Locate and identify every blood parasite.
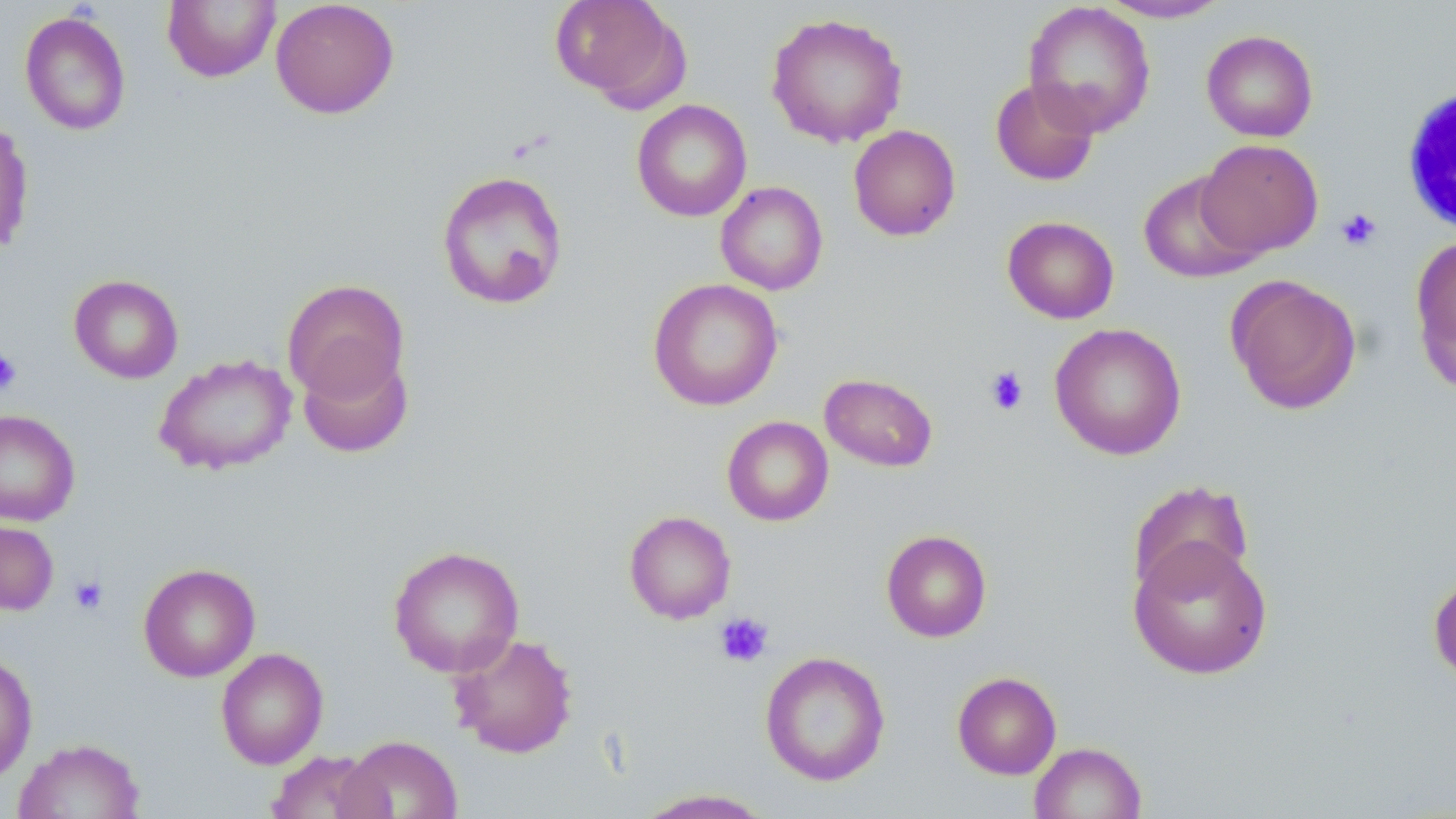
No blood parasites seen.

slide_level_diagnosis: no evidence of blood parasites
modality: optical microscopy
image_size: 1456×819 pixels
uninfected_red_blood_cell_locations: 'approximate bounding boxes as (x1, y1, x2, y2) in pixels: (162, 0, 281, 83), (270, 0, 399, 119), (549, 0, 686, 108), (1095, 1, 1233, 23), (1023, 2, 1156, 138), (20, 11, 131, 135), (765, 11, 909, 148), (1201, 29, 1318, 142), (989, 78, 1100, 187), (631, 99, 752, 222), (0, 116, 35, 258), (848, 124, 961, 241), (1196, 139, 1323, 258), (436, 170, 568, 310), (1137, 171, 1264, 283), (716, 181, 828, 296), (1002, 215, 1119, 324), (1410, 234, 1456, 394), (69, 274, 183, 384), (1225, 274, 1362, 415), (282, 278, 409, 403), (647, 278, 783, 411), (1049, 322, 1187, 461), (297, 347, 414, 458), (154, 353, 297, 476), (819, 373, 939, 472), (0, 409, 80, 526), (722, 416, 833, 526), (1127, 479, 1255, 600), (624, 510, 737, 624), (0, 518, 58, 616), (881, 529, 992, 642), (1128, 537, 1273, 679), (388, 545, 525, 677), (138, 562, 261, 682), (1428, 572, 1456, 686), (448, 632, 579, 759), (215, 647, 329, 769), (760, 651, 891, 786), (0, 653, 38, 785), (952, 671, 1062, 780), (338, 734, 463, 818), (13, 737, 145, 819), (1029, 741, 1146, 819), (265, 750, 385, 819), (631, 788, 777, 818)'
magnification: 1000x
platelet_locations: 'approximate bounding boxes as (x1, y1, x2, y2) in pixels: (1336, 207, 1382, 252), (0, 350, 21, 396), (984, 366, 1030, 416), (70, 575, 108, 615), (715, 612, 774, 667)'
stain: May-Grünwald-Giemsa
field_of_view: one of a larger specimen
white_blood_cell_locations: 'approximate bounding boxes as (x1, y1, x2, y2) in pixels: (1398, 83, 1456, 239)'
preparation: thin blood smear